Assess for Plasmodium parasites.
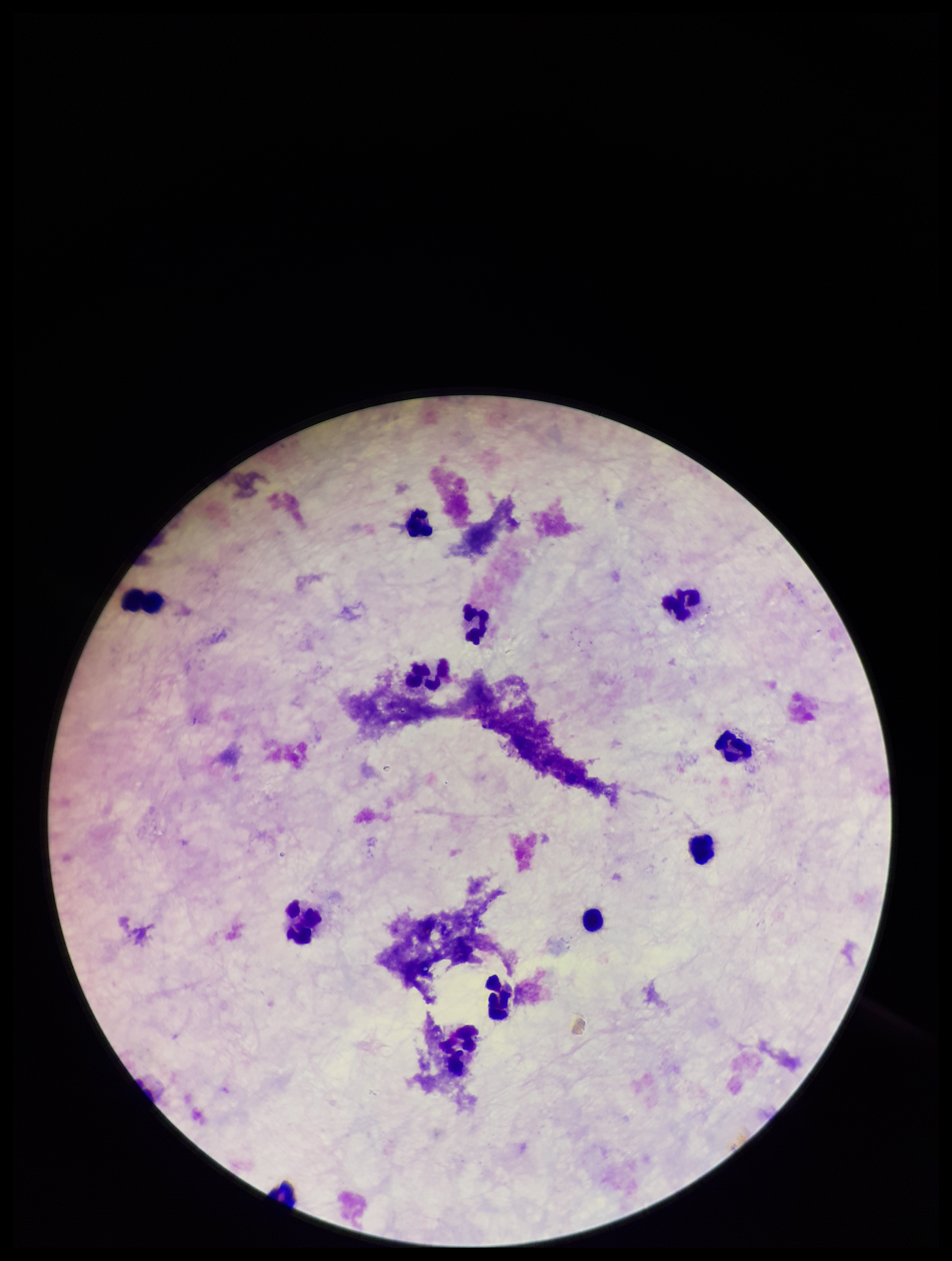
None detected.

Giemsa stain. Leukocyte count: 11. Patient malaria status: negative. Preparation: thick blood smear. Parasite count: 0. Smartphone photograph taken through the eyepiece of a microscope. Image is 952×1261 pixels. One field from this slide.